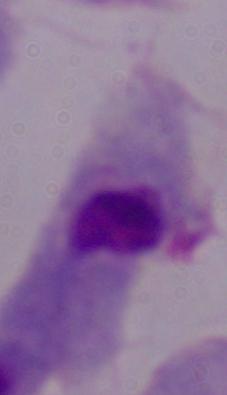

Captured at 1000x magnification. A trichomonad is seen. Photomicrograph.